Assess the morphology of the red blood cells.
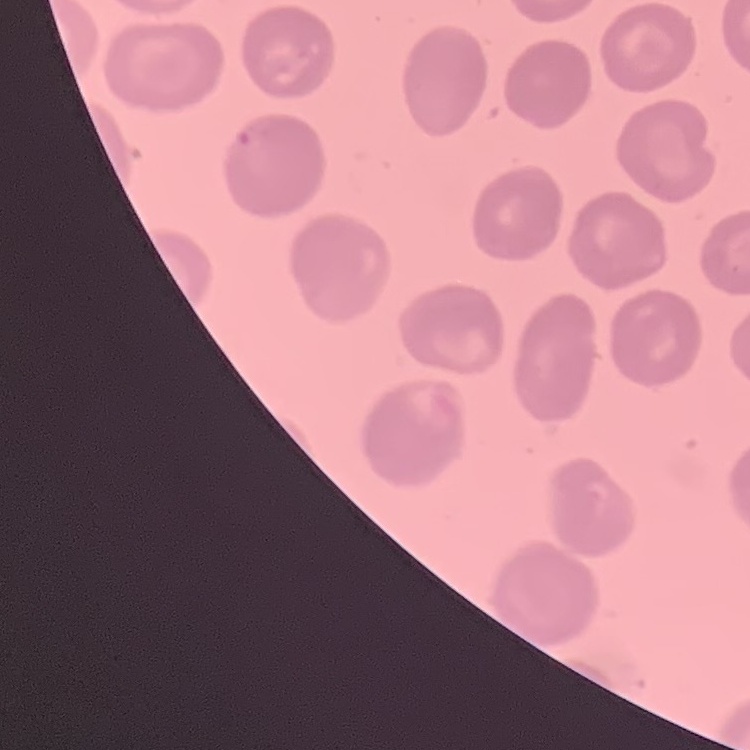

They show no rouleaux formation.

Summary:
  - Image type: square crop of a larger photomicrograph
  - Preparation: thin blood film
  - Stain: Field's or Giemsa